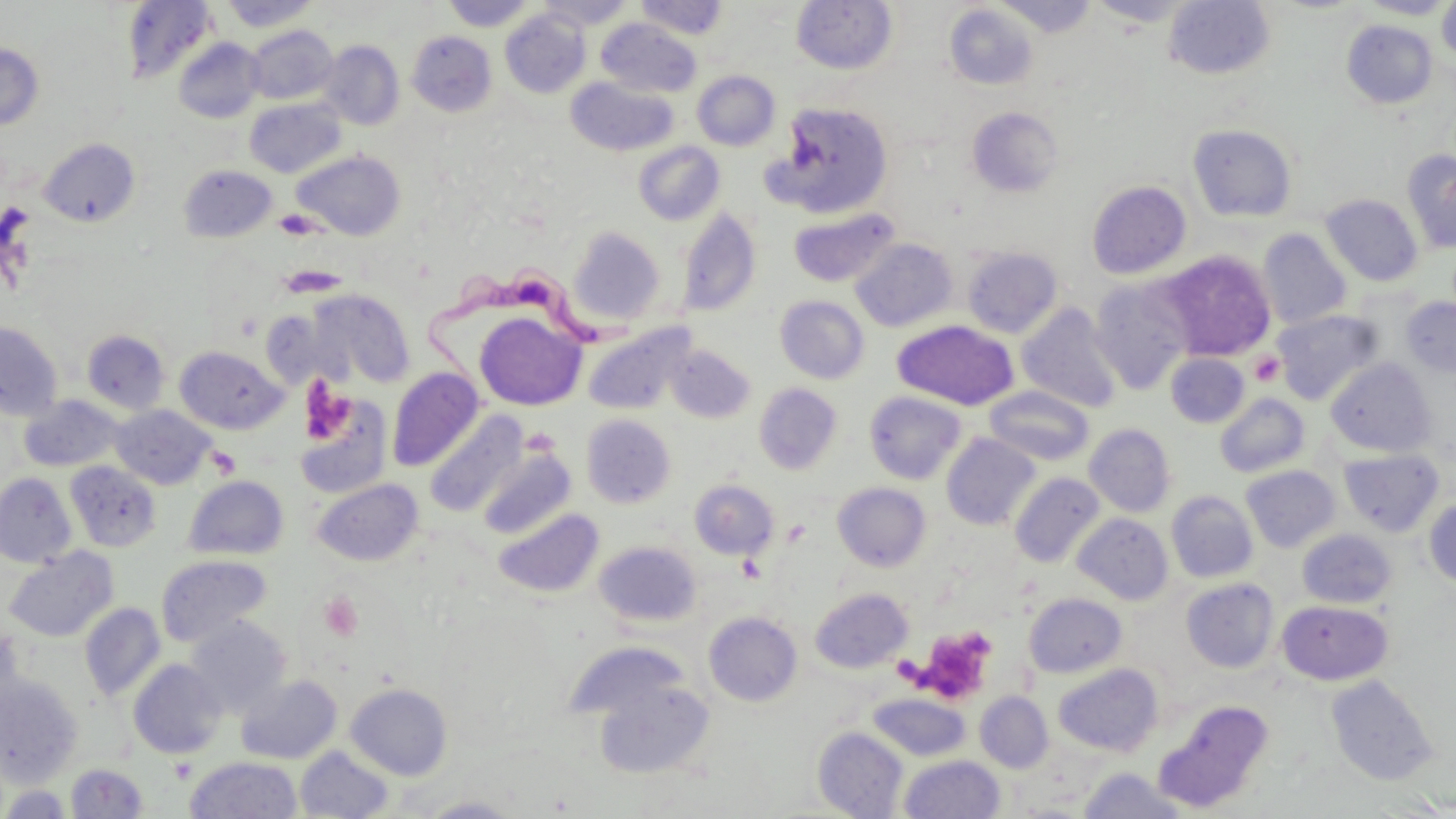

Approximate bounding boxes as (x1,y1)-(x2,y2) corner pairs in pixels. Trypanosoma brucei locations: (425,262)-(650,391). Uninfected red blood cell locations: (442,0)-(536,31), (538,0)-(635,30), (635,0)-(729,40), (791,0)-(897,74), (992,0)-(1101,38), (1086,0)-(1198,27), (1355,0)-(1455,20), (121,1)-(217,85), (219,1)-(320,32), (1163,1)-(1276,80), (1436,1)-(1456,63), (944,3)-(1039,89), (500,8)-(591,98), (597,19)-(702,97), (1342,20)-(1438,109), (245,25)-(338,104), (407,30)-(497,116), (173,37)-(265,123), (318,40)-(405,131), (0,44)-(43,130), (692,70)-(780,151), (566,77)-(678,156), (244,98)-(345,178), (768,101)-(894,217), (966,106)-(1064,198), (1187,123)-(1298,222), (39,138)-(140,227), (633,141)-(725,225), (1402,148)-(1456,254), (293,150)-(406,239), (178,164)-(277,242), (1086,180)-(1192,279), (1321,194)-(1423,286), (677,206)-(761,317), (787,206)-(900,287), (568,226)-(665,326), (1257,228)-(1353,328), (850,238)-(958,332), (961,246)-(1063,338), (1160,250)-(1276,361), (1089,278)-(1192,394), (308,289)-(414,387), (775,295)-(870,384), (1400,296)-(1456,378), (1016,302)-(1123,413), (1272,309)-(1384,405), (474,311)-(586,410), (892,319)-(1019,411), (0,321)-(63,421), (582,321)-(696,415), (82,329)-(170,414), (666,344)-(756,423), (175,345)-(288,435), (1165,353)-(1250,428), (1326,358)-(1438,457), (387,367)-(484,472), (754,383)-(842,475), (985,386)-(1094,466), (864,390)-(968,484), (1215,393)-(1310,478), (20,395)-(124,472), (294,397)-(393,498), (111,405)-(215,489), (425,411)-(528,516), (582,414)-(677,507), (1084,423)-(1176,517), (941,433)-(1041,530), (477,447)-(577,539), (1338,448)-(1444,537), (65,461)-(162,552), (1241,465)-(1340,552), (1010,472)-(1106,568), (0,473)-(77,568), (184,475)-(289,560), (313,478)-(423,565), (690,479)-(779,560), (832,482)-(931,572), (1166,490)-(1258,583), (1423,496)-(1456,590), (493,507)-(604,598), (1072,513)-(1173,605), (1298,529)-(1397,608), (594,540)-(701,628), (4,547)-(118,643), (155,554)-(272,647), (1181,578)-(1279,672), (810,588)-(913,673), (1023,592)-(1127,678), (1277,599)-(1393,685), (79,602)-(166,701), (704,612)-(802,706), (185,616)-(291,718), (0,624)-(25,717), (563,642)-(686,723), (128,659)-(227,759), (1053,663)-(1163,756), (0,674)-(83,785), (235,674)-(342,764), (1325,674)-(1439,785), (592,676)-(716,779), (345,683)-(453,780), (975,691)-(1053,772), (868,693)-(970,761), (1156,699)-(1275,812), (813,727)-(908,818), (294,746)-(395,818), (899,754)-(1005,818), (185,756)-(301,818), (66,762)-(148,817), (1077,768)-(1187,818), (1,785)-(73,818), (419,796)-(523,818). Platelet locations: (275,209)-(320,239), (1249,351)-(1285,386), (206,446)-(241,477), (318,592)-(364,641), (915,626)-(999,703). Slide-level diagnosis: Trypanosoma brucei. One field of a larger specimen. Thin blood film. May-Grünwald-Giemsa stain. Optical microscopy. Captured at 1000x magnification. Image is 1456×819 pixels.